Identify the blood parasite species.
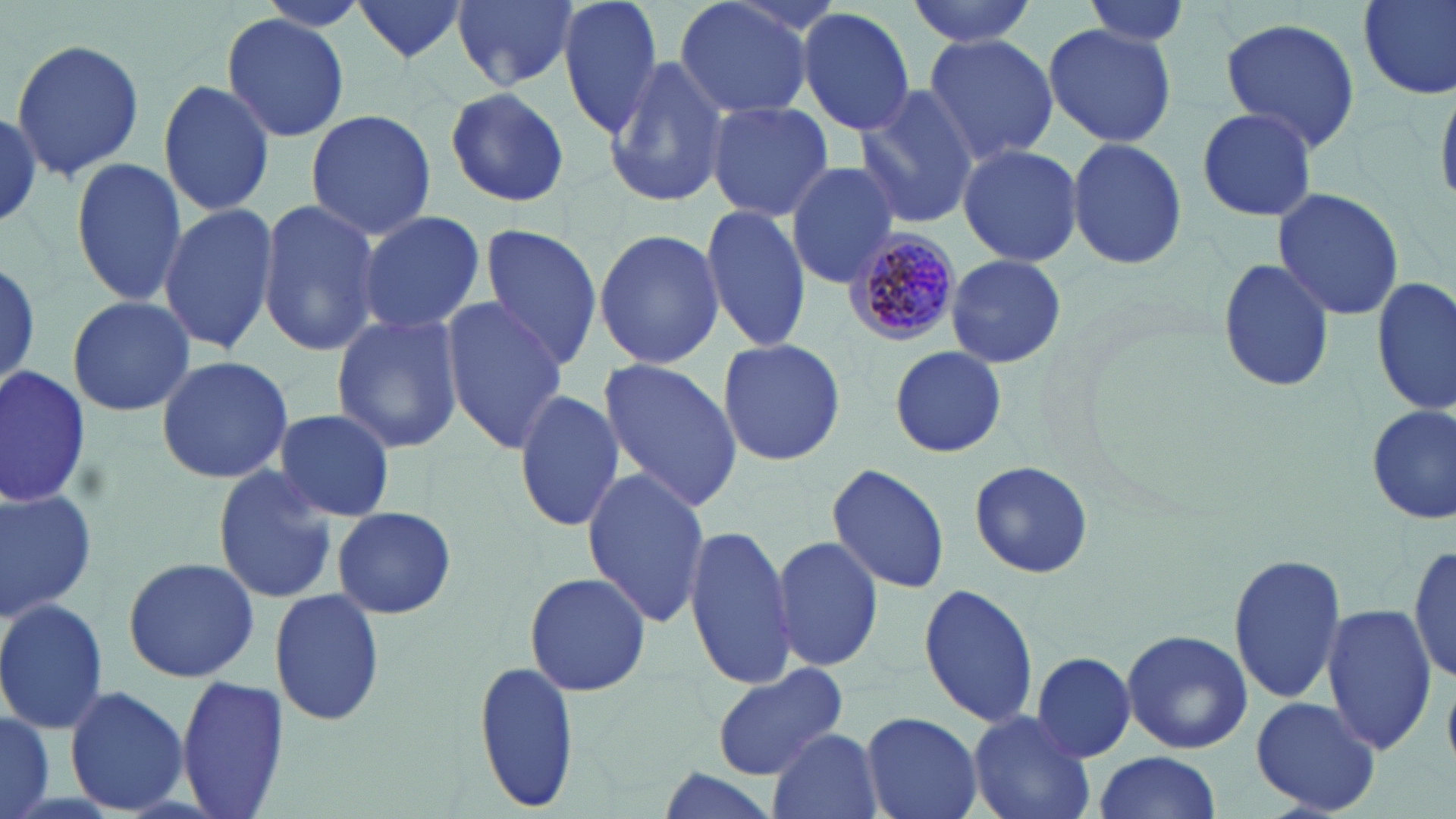

Plasmodium malariae.

Summary:
  - Coordinate format: approximate bounding boxes as named x1/y1/x2/y2 corners in pixels
  - Uninfected red blood cell locations: (x1=352, y1=0, x2=471, y2=64), (x1=454, y1=0, x2=579, y2=91), (x1=557, y1=0, x2=663, y2=141), (x1=672, y1=0, x2=818, y2=122), (x1=907, y1=0, x2=1037, y2=48), (x1=1081, y1=0, x2=1196, y2=51), (x1=1358, y1=0, x2=1456, y2=99), (x1=797, y1=8, x2=917, y2=138), (x1=221, y1=12, x2=350, y2=140), (x1=1217, y1=15, x2=1360, y2=152), (x1=1042, y1=22, x2=1176, y2=147), (x1=920, y1=33, x2=1061, y2=166), (x1=9, y1=39, x2=147, y2=182), (x1=605, y1=55, x2=730, y2=209), (x1=156, y1=78, x2=275, y2=216), (x1=1436, y1=79, x2=1456, y2=212), (x1=854, y1=85, x2=980, y2=232), (x1=444, y1=87, x2=573, y2=208), (x1=706, y1=101, x2=835, y2=220), (x1=1193, y1=105, x2=1320, y2=224), (x1=0, y1=109, x2=44, y2=228), (x1=304, y1=109, x2=438, y2=240), (x1=1066, y1=134, x2=1187, y2=270), (x1=956, y1=142, x2=1085, y2=268), (x1=70, y1=157, x2=187, y2=308), (x1=786, y1=161, x2=903, y2=287), (x1=1272, y1=188, x2=1405, y2=322), (x1=257, y1=199, x2=380, y2=359), (x1=157, y1=201, x2=278, y2=356), (x1=699, y1=205, x2=809, y2=355), (x1=357, y1=210, x2=485, y2=337), (x1=477, y1=223, x2=603, y2=368), (x1=593, y1=229, x2=726, y2=368), (x1=946, y1=254, x2=1066, y2=368), (x1=0, y1=257, x2=41, y2=388), (x1=1216, y1=257, x2=1336, y2=395), (x1=1372, y1=279, x2=1454, y2=415), (x1=66, y1=295, x2=194, y2=418), (x1=442, y1=298, x2=568, y2=453), (x1=331, y1=313, x2=465, y2=453), (x1=716, y1=336, x2=848, y2=467), (x1=888, y1=344, x2=1007, y2=460), (x1=155, y1=354, x2=295, y2=485), (x1=597, y1=358, x2=742, y2=515), (x1=0, y1=368, x2=90, y2=509), (x1=512, y1=385, x2=624, y2=536), (x1=1365, y1=402, x2=1456, y2=526), (x1=270, y1=407, x2=397, y2=522), (x1=969, y1=461, x2=1094, y2=578), (x1=826, y1=462, x2=951, y2=595), (x1=208, y1=465, x2=337, y2=604), (x1=580, y1=467, x2=712, y2=628), (x1=0, y1=483, x2=96, y2=619), (x1=333, y1=505, x2=458, y2=619), (x1=682, y1=523, x2=799, y2=689), (x1=769, y1=532, x2=885, y2=676), (x1=1408, y1=540, x2=1454, y2=688), (x1=1226, y1=550, x2=1347, y2=707), (x1=122, y1=554, x2=261, y2=684), (x1=522, y1=569, x2=654, y2=699), (x1=918, y1=581, x2=1040, y2=731), (x1=268, y1=590, x2=386, y2=727), (x1=0, y1=598, x2=108, y2=734), (x1=1321, y1=604, x2=1435, y2=756), (x1=1122, y1=629, x2=1253, y2=755), (x1=1028, y1=651, x2=1138, y2=762), (x1=474, y1=659, x2=581, y2=811), (x1=711, y1=663, x2=848, y2=778), (x1=175, y1=677, x2=290, y2=818), (x1=63, y1=684, x2=190, y2=815), (x1=1250, y1=695, x2=1382, y2=816), (x1=0, y1=707, x2=56, y2=819), (x1=967, y1=710, x2=1096, y2=819), (x1=860, y1=711, x2=983, y2=819), (x1=768, y1=728, x2=883, y2=819), (x1=1090, y1=751, x2=1222, y2=818), (x1=653, y1=769, x2=783, y2=819)
  - Plasmodium malariae-infected red blood cell locations: (x1=846, y1=227, x2=964, y2=346)
  - Image size: 1456×819 pixels
  - Preparation: thin blood smear
  - Modality: light microscopy
  - Stain: May-Grünwald-Giemsa
  - Magnification: 1000x
  - Field of view: single